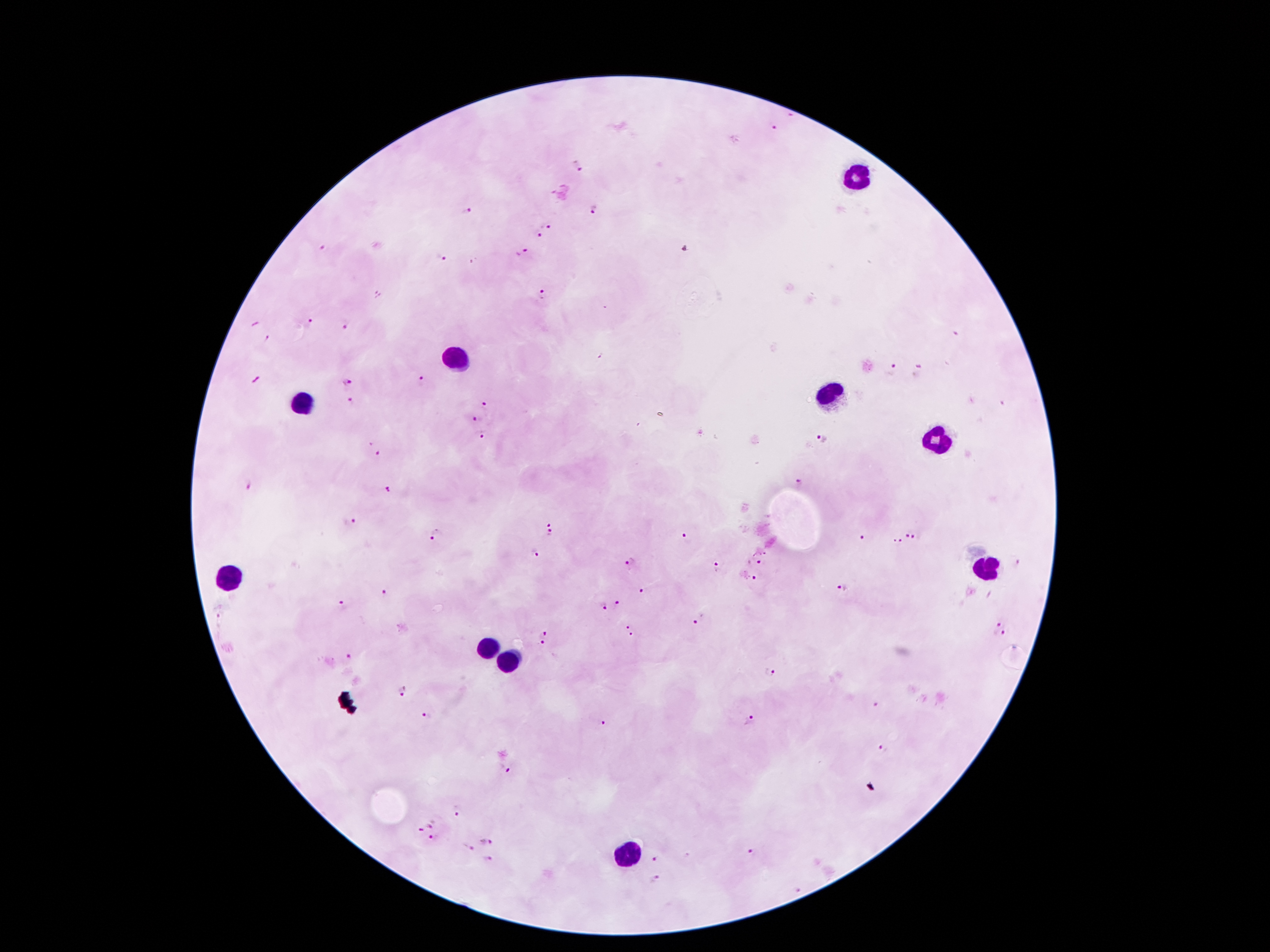
Approximate object centers, in pixels from the top-left corner. Malaria parasite locations: (x=772, y=127), (x=576, y=167), (x=597, y=209), (x=463, y=212), (x=548, y=225), (x=537, y=234), (x=684, y=250), (x=522, y=254), (x=442, y=258), (x=378, y=293), (x=541, y=296), (x=310, y=320), (x=345, y=325), (x=264, y=338), (x=890, y=372), (x=918, y=373), (x=348, y=382), (x=422, y=382), (x=350, y=403), (x=487, y=404), (x=478, y=419), (x=481, y=433), (x=823, y=439), (x=379, y=454), (x=796, y=482), (x=247, y=486), (x=389, y=489), (x=548, y=522), (x=351, y=523), (x=904, y=530), (x=918, y=534), (x=438, y=535), (x=551, y=535), (x=688, y=539), (x=862, y=540), (x=900, y=543), (x=533, y=552), (x=764, y=552), (x=1019, y=561), (x=631, y=563), (x=753, y=563), (x=719, y=570), (x=749, y=579), (x=842, y=587), (x=642, y=591), (x=386, y=594), (x=343, y=604), (x=617, y=605), (x=604, y=609), (x=701, y=620), (x=993, y=623), (x=630, y=629), (x=543, y=634), (x=1006, y=635), (x=542, y=646), (x=348, y=658), (x=769, y=673), (x=401, y=692), (x=878, y=705), (x=426, y=716), (x=751, y=722), (x=603, y=723), (x=882, y=749), (x=510, y=772), (x=458, y=811), (x=433, y=824), (x=419, y=831), (x=434, y=839), (x=488, y=841), (x=466, y=847), (x=752, y=852), (x=652, y=858), (x=487, y=859), (x=657, y=879), (x=801, y=890). Leukocyte locations: (x=857, y=173), (x=456, y=363), (x=830, y=396), (x=301, y=402), (x=935, y=437), (x=987, y=568), (x=229, y=580), (x=488, y=647), (x=509, y=664), (x=628, y=856). One field from this slide. Image is 1270×952 pixels. Giemsa stain. Patient malaria status: positive for Plasmodium falciparum. Thick blood smear. 100x magnification. Smartphone photograph taken through the microscope eyepiece.